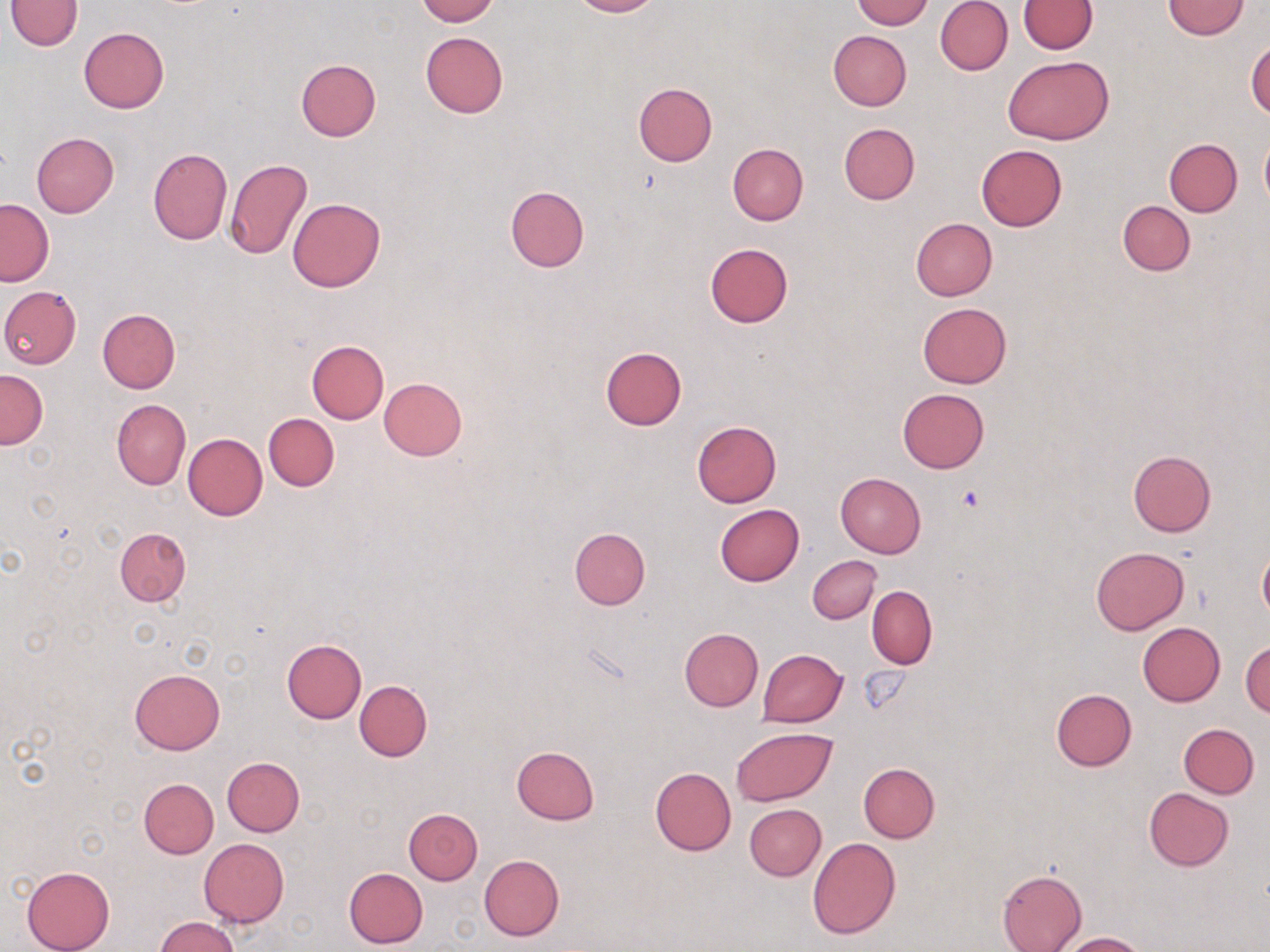

Summary:
  - Coordinate format: approximate bounding boxes as (x1, y1, x2, y2) in pixels
  - Uninfected red blood cell locations: (6, 0, 83, 51), (414, 0, 498, 24), (567, 0, 658, 17), (852, 0, 932, 29), (935, 0, 1013, 75), (1019, 0, 1097, 54), (1163, 1, 1251, 39), (78, 26, 169, 114), (828, 30, 911, 111), (420, 32, 508, 118), (1246, 36, 1270, 120), (1003, 55, 1112, 144), (295, 58, 380, 142), (633, 82, 717, 166), (838, 123, 919, 204), (31, 131, 119, 217), (1260, 134, 1270, 209), (1163, 139, 1242, 216), (726, 143, 808, 225), (976, 144, 1067, 230), (147, 146, 232, 245), (225, 159, 313, 259), (505, 185, 589, 273), (1, 199, 54, 286), (288, 199, 385, 293), (1117, 200, 1195, 276), (910, 217, 998, 301), (705, 242, 793, 326), (0, 285, 82, 368), (917, 302, 1011, 388), (98, 309, 180, 393), (308, 342, 388, 422), (600, 345, 687, 431), (0, 370, 48, 448), (379, 377, 467, 460), (897, 388, 989, 472), (112, 399, 190, 491), (263, 413, 338, 491), (691, 420, 781, 507), (183, 433, 267, 520), (1128, 449, 1216, 536), (834, 472, 926, 558), (714, 503, 804, 586), (569, 526, 650, 609), (115, 527, 191, 606), (1090, 546, 1189, 635), (1258, 546, 1270, 625), (807, 555, 881, 624), (867, 587, 937, 668), (1137, 622, 1225, 706), (679, 627, 763, 711), (281, 639, 365, 723), (1241, 639, 1269, 717), (757, 649, 848, 728), (131, 667, 224, 754), (354, 680, 432, 761), (1051, 688, 1137, 771), (1179, 723, 1259, 798), (731, 726, 838, 806), (510, 746, 600, 825), (222, 756, 305, 836), (858, 762, 940, 842), (650, 766, 736, 855), (139, 778, 218, 858), (1143, 787, 1234, 871), (744, 803, 826, 880), (403, 809, 482, 884), (807, 838, 900, 940), (198, 839, 289, 927), (479, 854, 564, 941), (21, 865, 115, 952), (343, 866, 428, 948), (997, 869, 1087, 952), (154, 917, 240, 952), (1058, 932, 1147, 951)
  - Platelet locations: (958, 484, 985, 512), (860, 667, 912, 715)
  - Slide-level diagnosis: negative for blood parasites
  - Modality: optical microscopy
  - Image size: 1270×952 pixels
  - Preparation: thin blood smear
  - Magnification: 1000x
  - Field of view: single
  - Stain: May-Grünwald-Giemsa